Report the malaria status of this cell.
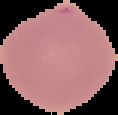

It is uninfected.

Image is 118×115 pixels. From a thin blood film. Cell region segmented out of the field of view; the surrounding area is masked to black.